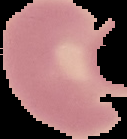
image_type: segmented cell region with the area outside set to black
image_size: 127×139 pixels
malaria_status: uninfected
preparation: thin blood smear